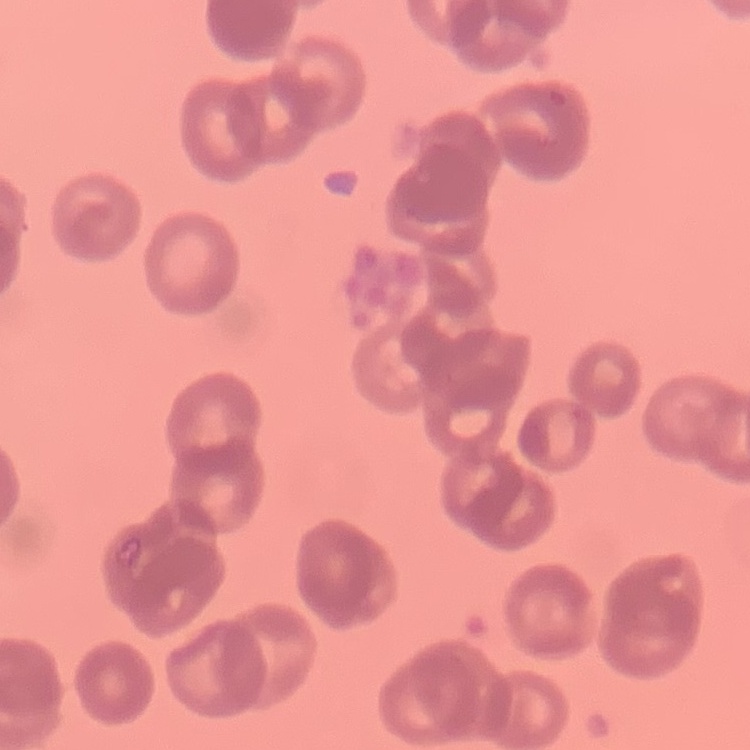

Summary:
  - Red blood cell morphology: rouleaux formation
  - Preparation: thin peripheral smear
  - Stain: Field's or Giemsa
  - Image type: one tile cut from a larger photomicrograph